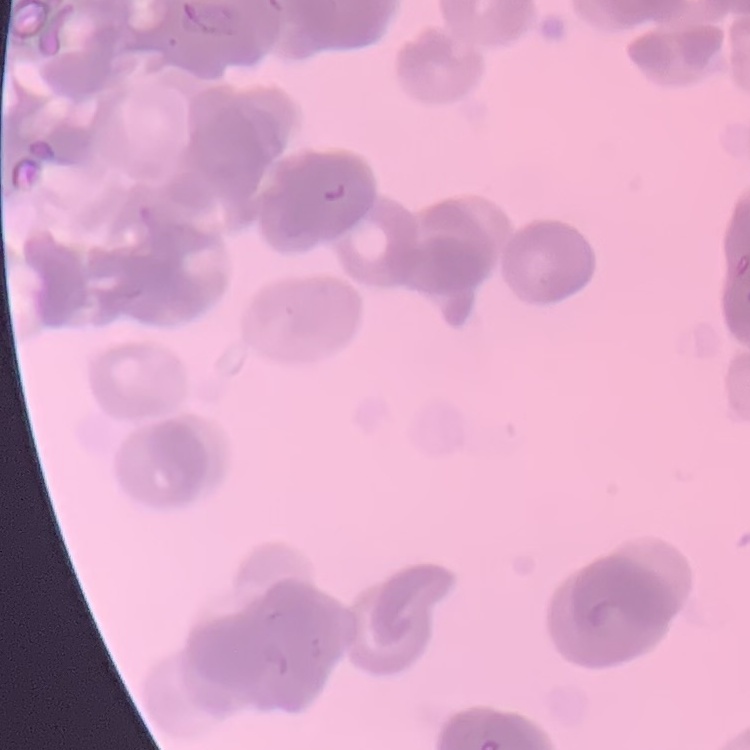

The erythrocytes show rouleaux formation. Square crop of a larger photomicrograph. Field's or Giemsa stain. Thin blood smear.